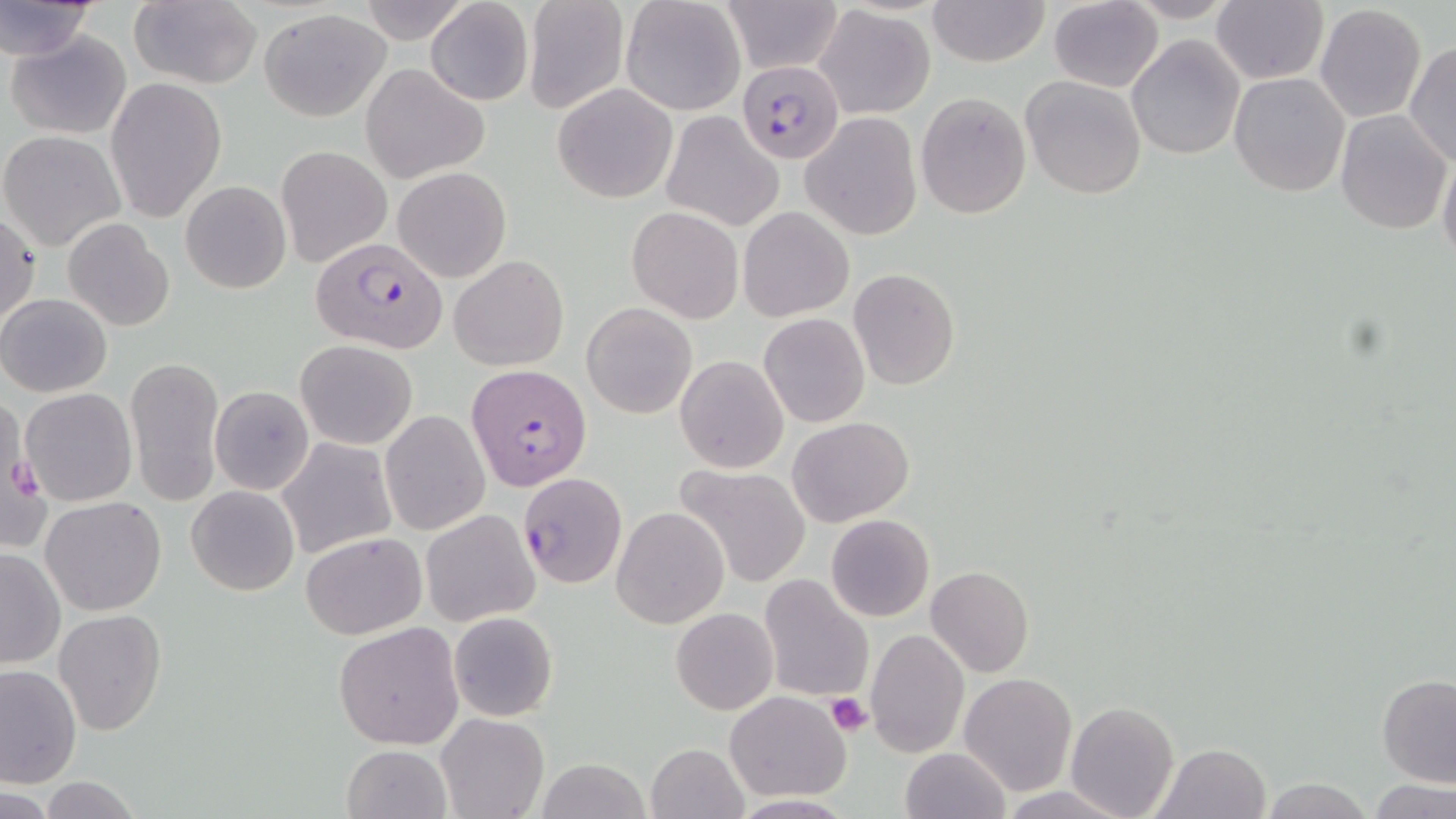
slide_level_diagnosis: Plasmodium falciparum
magnification: 1000x
modality: optical microscopy
uninfected_red_blood_cell_locations: 'approximate bounding boxes as (x1,y1)-(x2,y2) corner pairs in pixels: (358,0)-(472,45), (719,0)-(845,74), (928,0)-(1049,68), (1211,0)-(1328,86), (0,1)-(99,61), (128,1)-(261,89), (426,1)-(534,107), (522,1)-(629,115), (620,1)-(745,116), (1047,1)-(1164,90), (1315,4)-(1427,124), (812,5)-(936,120), (258,8)-(390,120), (6,32)-(132,138), (1126,35)-(1245,160), (1405,41)-(1455,165), (361,63)-(489,183), (1228,72)-(1350,197), (107,75)-(227,222), (1020,75)-(1148,200), (552,83)-(678,203), (915,90)-(1033,221), (1335,109)-(1452,232), (659,112)-(783,233), (801,112)-(924,240), (1,129)-(127,251), (278,144)-(391,267), (1437,149)-(1456,268), (392,167)-(511,283), (180,179)-(292,294), (628,206)-(744,322), (738,206)-(855,322), (0,211)-(41,329), (63,219)-(173,332), (449,254)-(568,371), (848,267)-(960,390), (1,293)-(112,397), (582,301)-(698,419), (758,313)-(870,427), (296,339)-(419,449), (125,355)-(224,508), (675,355)-(789,474), (210,385)-(315,496), (19,388)-(137,507), (379,408)-(490,536), (787,417)-(913,528), (276,438)-(396,558), (677,463)-(814,590), (517,473)-(629,591), (186,484)-(301,596), (40,496)-(167,616), (612,505)-(729,629), (420,508)-(540,626), (825,513)-(935,622), (301,531)-(425,640), (0,548)-(66,669), (925,566)-(1034,678), (758,574)-(873,705), (669,607)-(778,715), (54,608)-(166,735), (449,611)-(558,721), (333,621)-(465,750), (865,628)-(968,757), (0,664)-(81,788), (959,672)-(1078,796), (1377,673)-(1456,787), (726,693)-(849,803), (1065,701)-(1179,819), (436,713)-(549,819), (645,743)-(748,819), (1151,743)-(1272,819), (342,745)-(450,819), (900,747)-(1012,819), (535,758)-(655,819), (37,777)-(146,818), (1260,779)-(1374,817), (1369,780)-(1456,818)'
field_of_view: one of a larger specimen
platelet_locations: 'approximate bounding boxes as (x1,y1)-(x2,y2) corner pairs in pixels: (826,692)-(874,737)'
plasmodium_falciparum_infected_red_blood_cell_locations: 'approximate bounding boxes as (x1,y1)-(x2,y2) corner pairs in pixels: (737,59)-(844,164), (312,240)-(447,350), (466,363)-(592,491)'
preparation: thin blood film
stain: May-Grünwald-Giemsa
image_size: 1456×819 pixels